Comment on the morphology of the erythrocytes.
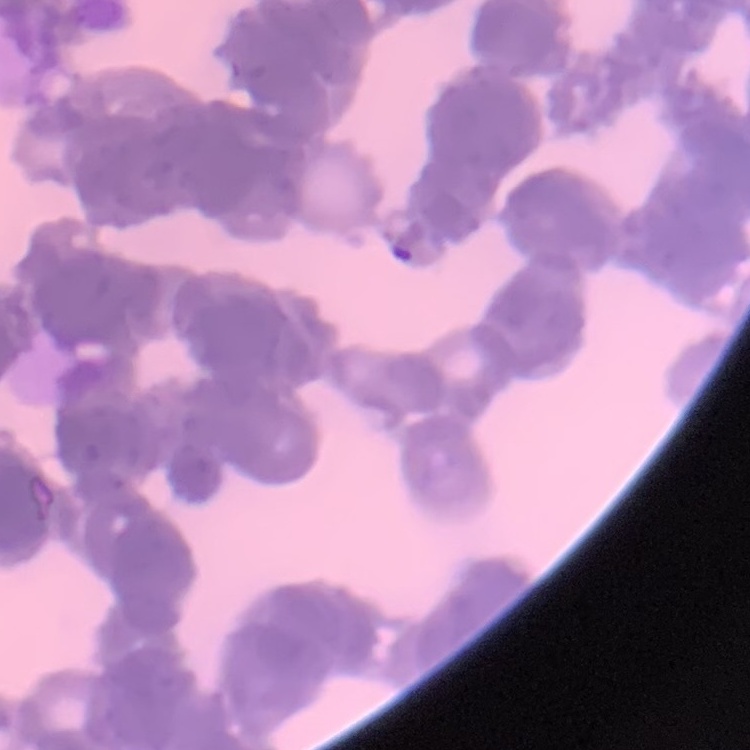
Rouleaux formation.

Thin blood film. Field's or Giemsa stain. One tile cut from a larger photomicrograph.